Name the parasite shown.
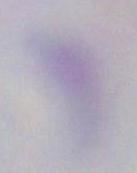
This is Toxoplasma gondii.

{
  "modality": "photomicrograph",
  "magnification": "1000x"
}